Point out each Plasmodium parasite.
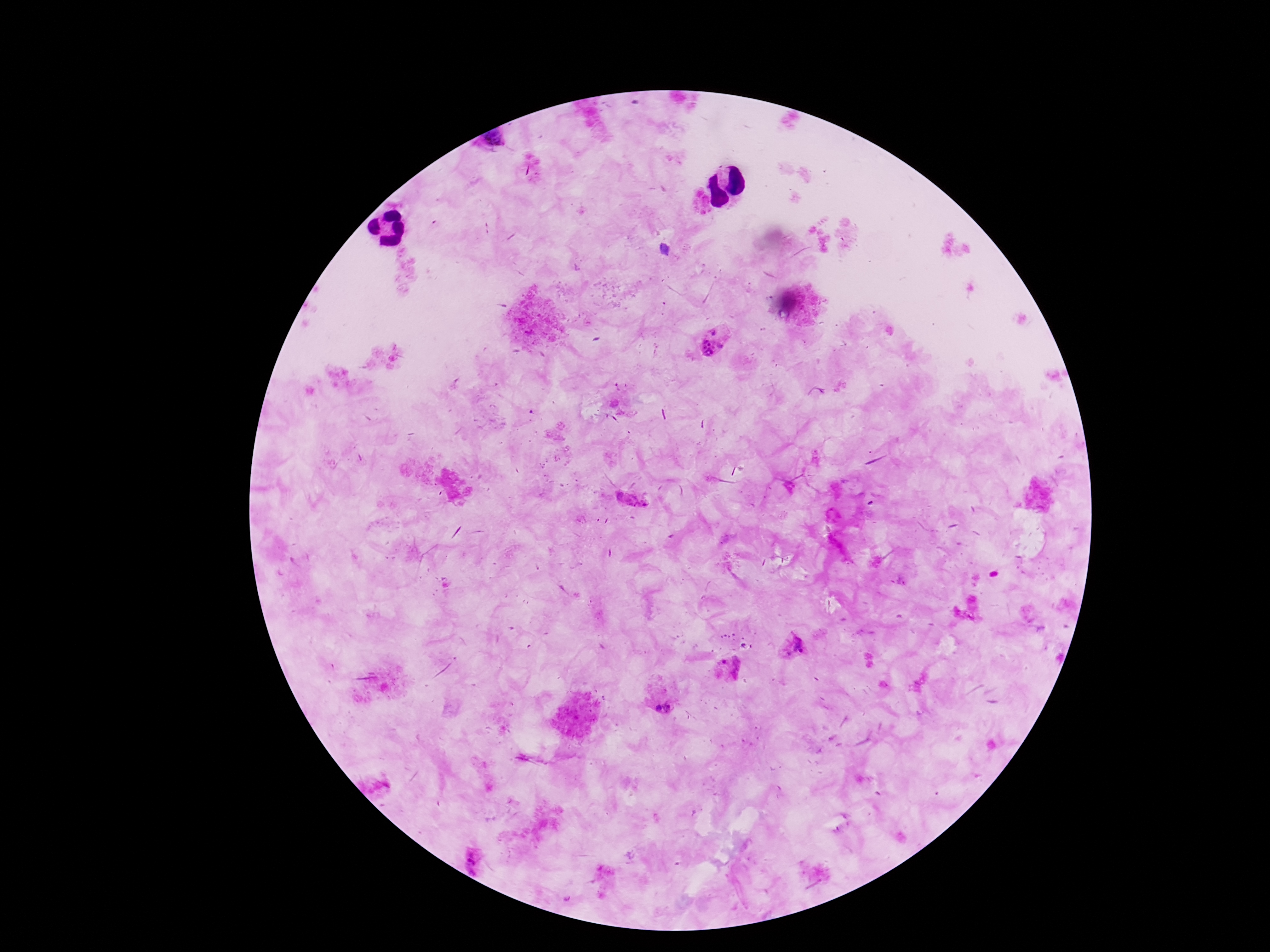

Approximate centers as [x, y] in pixels.
Plasmodium parasites: [493, 140], [715, 332], [711, 349], [631, 503], [968, 609], [794, 648], [729, 669], [669, 706], [657, 708], [474, 862].

capture = smartphone camera through the microscope eyepiece
stain = Giemsa
preparation = thick blood smear
field of view = one from this slide
image size = 1270×952 pixels
magnification = 100x
patient malaria status = positive